Outline each uninfected red blood cell.
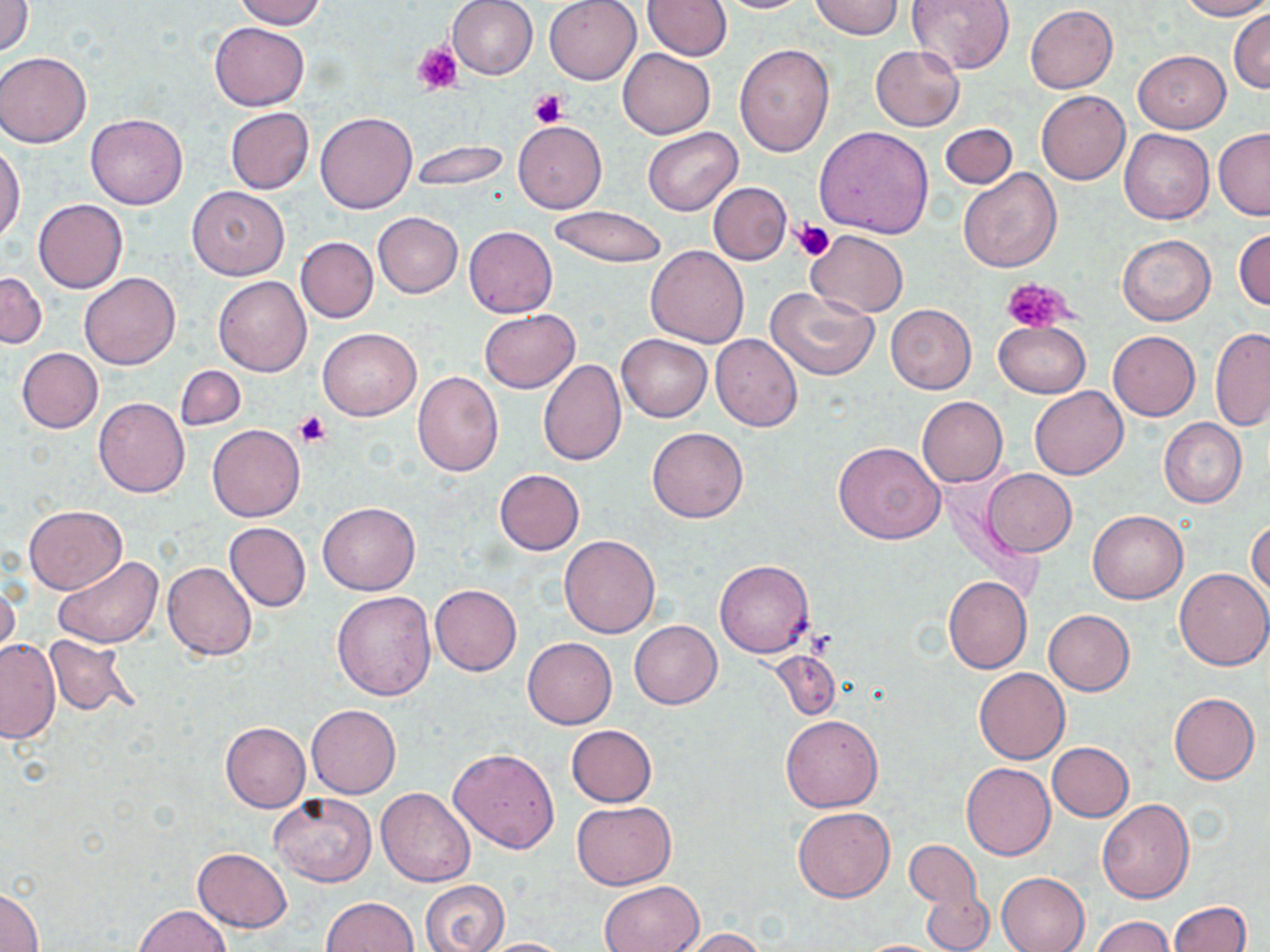
Approximate bounding boxes as named x1/y1/x2/y2 corners in pixels.
Uninfected red blood cells: (x1=233, y1=0, x2=327, y2=28), (x1=446, y1=0, x2=538, y2=80), (x1=544, y1=0, x2=641, y2=84), (x1=641, y1=0, x2=731, y2=59), (x1=716, y1=0, x2=813, y2=14), (x1=809, y1=0, x2=902, y2=39), (x1=907, y1=0, x2=1016, y2=73), (x1=1178, y1=0, x2=1270, y2=20), (x1=1, y1=1, x2=33, y2=58), (x1=1025, y1=4, x2=1118, y2=93), (x1=1229, y1=9, x2=1270, y2=93), (x1=209, y1=22, x2=309, y2=112), (x1=735, y1=44, x2=835, y2=156), (x1=870, y1=45, x2=964, y2=133), (x1=617, y1=47, x2=716, y2=138), (x1=1133, y1=50, x2=1230, y2=132), (x1=1, y1=52, x2=91, y2=148), (x1=1036, y1=91, x2=1130, y2=185), (x1=223, y1=107, x2=315, y2=194), (x1=315, y1=111, x2=417, y2=213), (x1=86, y1=113, x2=188, y2=210), (x1=513, y1=121, x2=606, y2=214), (x1=940, y1=122, x2=1017, y2=188), (x1=643, y1=126, x2=742, y2=215), (x1=816, y1=126, x2=935, y2=239), (x1=1214, y1=128, x2=1270, y2=220), (x1=1120, y1=129, x2=1215, y2=225), (x1=411, y1=140, x2=510, y2=191), (x1=0, y1=142, x2=26, y2=243), (x1=957, y1=167, x2=1063, y2=272), (x1=708, y1=182, x2=792, y2=263), (x1=186, y1=185, x2=290, y2=280), (x1=34, y1=199, x2=127, y2=293), (x1=548, y1=206, x2=668, y2=267), (x1=373, y1=212, x2=463, y2=297), (x1=464, y1=226, x2=557, y2=317), (x1=1234, y1=228, x2=1270, y2=312), (x1=805, y1=230, x2=907, y2=318), (x1=1117, y1=234, x2=1215, y2=326), (x1=296, y1=237, x2=378, y2=323), (x1=645, y1=246, x2=749, y2=348), (x1=0, y1=272, x2=46, y2=349), (x1=80, y1=272, x2=180, y2=369), (x1=213, y1=275, x2=311, y2=376), (x1=765, y1=287, x2=878, y2=380), (x1=885, y1=305, x2=976, y2=394), (x1=479, y1=309, x2=580, y2=392), (x1=994, y1=320, x2=1090, y2=398), (x1=1210, y1=327, x2=1270, y2=431), (x1=318, y1=328, x2=422, y2=421), (x1=1108, y1=331, x2=1200, y2=420), (x1=616, y1=333, x2=712, y2=422), (x1=710, y1=334, x2=803, y2=433), (x1=16, y1=348, x2=103, y2=433), (x1=537, y1=359, x2=625, y2=466), (x1=176, y1=365, x2=245, y2=430), (x1=412, y1=371, x2=503, y2=476), (x1=1029, y1=386, x2=1127, y2=479), (x1=917, y1=396, x2=1008, y2=486), (x1=94, y1=397, x2=189, y2=497), (x1=1160, y1=419, x2=1247, y2=508), (x1=207, y1=424, x2=305, y2=521), (x1=648, y1=427, x2=749, y2=523), (x1=833, y1=441, x2=945, y2=544), (x1=982, y1=468, x2=1076, y2=557), (x1=494, y1=469, x2=585, y2=554), (x1=317, y1=502, x2=421, y2=595), (x1=23, y1=505, x2=126, y2=594), (x1=1088, y1=510, x2=1188, y2=603), (x1=1247, y1=518, x2=1270, y2=596), (x1=224, y1=522, x2=311, y2=611), (x1=559, y1=534, x2=660, y2=638), (x1=53, y1=556, x2=162, y2=648), (x1=714, y1=559, x2=815, y2=658), (x1=162, y1=561, x2=257, y2=660), (x1=1175, y1=567, x2=1270, y2=671), (x1=943, y1=576, x2=1032, y2=673), (x1=0, y1=579, x2=19, y2=661), (x1=429, y1=585, x2=522, y2=676), (x1=332, y1=590, x2=436, y2=701), (x1=1043, y1=609, x2=1135, y2=694), (x1=629, y1=620, x2=722, y2=709), (x1=44, y1=635, x2=139, y2=717), (x1=524, y1=637, x2=616, y2=729), (x1=1, y1=638, x2=60, y2=744), (x1=770, y1=650, x2=841, y2=720), (x1=974, y1=668, x2=1069, y2=764), (x1=1168, y1=691, x2=1260, y2=785), (x1=306, y1=705, x2=401, y2=797), (x1=782, y1=714, x2=882, y2=812), (x1=221, y1=721, x2=310, y2=812), (x1=565, y1=724, x2=657, y2=807), (x1=1047, y1=742, x2=1134, y2=821), (x1=448, y1=748, x2=559, y2=853), (x1=961, y1=763, x2=1056, y2=860), (x1=375, y1=787, x2=475, y2=887), (x1=269, y1=793, x2=378, y2=886), (x1=1097, y1=799, x2=1195, y2=903), (x1=572, y1=801, x2=675, y2=890), (x1=792, y1=807, x2=895, y2=903), (x1=905, y1=841, x2=984, y2=922), (x1=193, y1=848, x2=292, y2=932), (x1=996, y1=872, x2=1089, y2=952), (x1=420, y1=880, x2=509, y2=952), (x1=599, y1=881, x2=704, y2=952), (x1=919, y1=881, x2=993, y2=951), (x1=1, y1=887, x2=43, y2=951), (x1=323, y1=896, x2=419, y2=952), (x1=1168, y1=901, x2=1251, y2=952), (x1=135, y1=905, x2=233, y2=951), (x1=1092, y1=916, x2=1175, y2=952), (x1=678, y1=928, x2=768, y2=951), (x1=476, y1=937, x2=573, y2=951), (x1=853, y1=939, x2=950, y2=951).

Platelet locations: (x1=413, y1=43, x2=462, y2=96), (x1=528, y1=89, x2=568, y2=126), (x1=793, y1=220, x2=836, y2=262), (x1=1001, y1=277, x2=1077, y2=334), (x1=294, y1=411, x2=331, y2=447). Slide-level diagnosis: negative for blood parasites. Light microscopy. Thin blood film. Captured at 1000x magnification. One field of a larger specimen. Image is 1270×952 pixels. May-Grünwald-Giemsa-stained preparation.